Assess this cell for malaria.
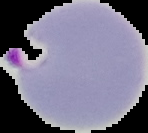
It is parasitized.

Cell region segmented out of the field of view; the surrounding area is masked to black. From a thin blood smear. Image is 148×133 pixels.